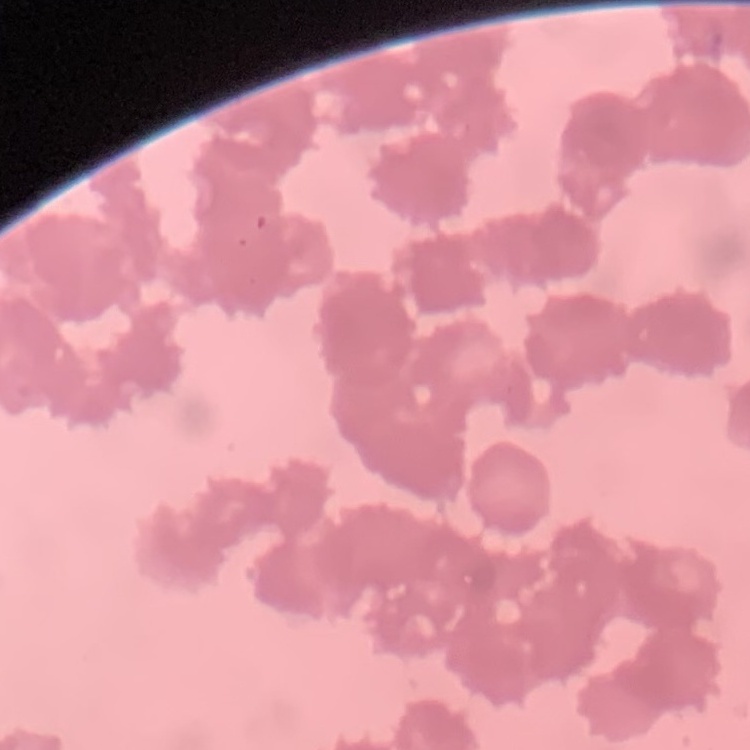

Summary:
  - Erythrocyte morphology: rouleaux formation
  - Image type: square crop of a larger photomicrograph
  - Stain: Field's or Giemsa
  - Preparation: thin peripheral smear